Report the malaria status of this cell.
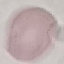
Uninfected.

Giemsa stain. Acquired by smartphone through the microscope eyepiece. Automatically extracted cell patch, resized to 64 × 64 pixels. Thin blood film.